Assess the morphology of the erythrocytes.
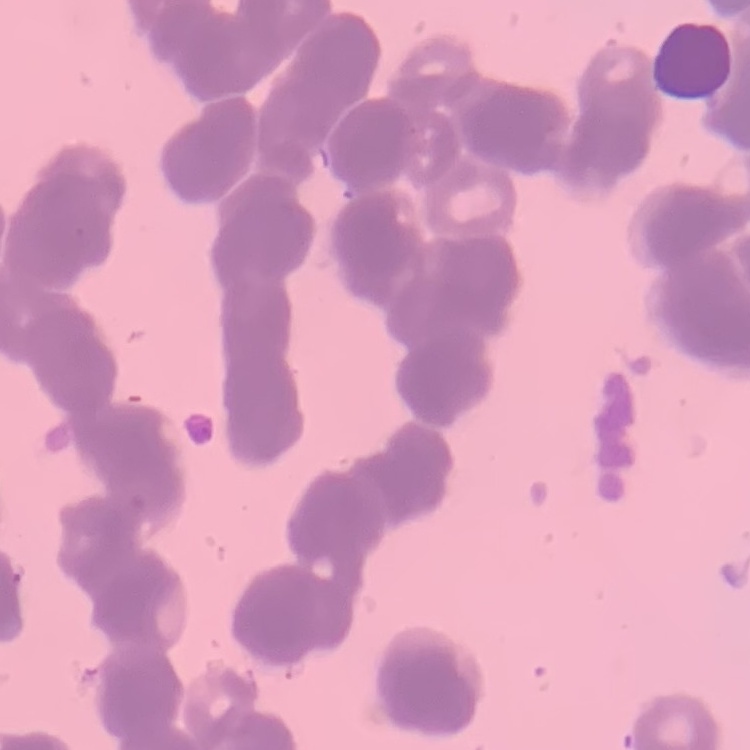

They show rouleaux formation.

One tile cut from a larger photomicrograph. Thin blood smear. Field's or Giemsa stain.